Identify the blood parasite species.
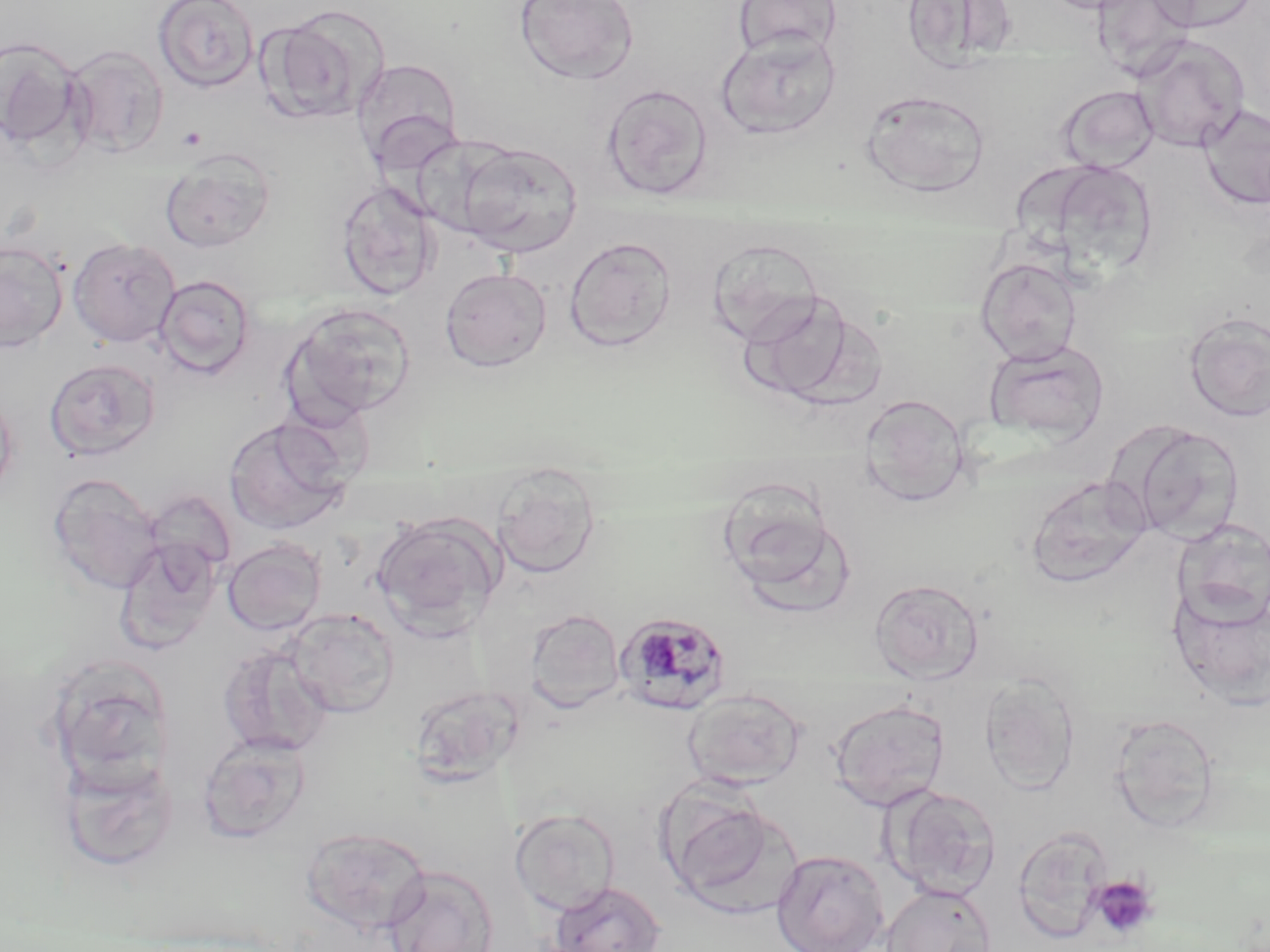

Plasmodium malariae.

Approximate bounding boxes as named x1/y1/x2/y2 corners in pixels. Plasmodium malariae-infected red blood cell locations: (x1=617, y1=611, x2=732, y2=716). Platelet locations: (x1=1087, y1=875, x2=1159, y2=942). Uninfected red blood cell locations: (x1=153, y1=0, x2=259, y2=93), (x1=514, y1=0, x2=638, y2=84), (x1=732, y1=0, x2=842, y2=59), (x1=901, y1=0, x2=1018, y2=72), (x1=1038, y1=0, x2=1149, y2=14), (x1=1091, y1=0, x2=1197, y2=81), (x1=1147, y1=0, x2=1260, y2=33), (x1=261, y1=7, x2=388, y2=126), (x1=717, y1=32, x2=841, y2=140), (x1=1132, y1=35, x2=1249, y2=152), (x1=0, y1=36, x2=85, y2=154), (x1=64, y1=44, x2=169, y2=158), (x1=350, y1=58, x2=464, y2=171), (x1=600, y1=83, x2=715, y2=200), (x1=1058, y1=85, x2=1159, y2=173), (x1=861, y1=90, x2=991, y2=197), (x1=1198, y1=104, x2=1270, y2=210), (x1=410, y1=133, x2=519, y2=238), (x1=457, y1=142, x2=583, y2=258), (x1=159, y1=148, x2=275, y2=253), (x1=1045, y1=161, x2=1158, y2=276), (x1=334, y1=180, x2=441, y2=300), (x1=563, y1=236, x2=677, y2=352), (x1=68, y1=237, x2=181, y2=348), (x1=707, y1=237, x2=824, y2=347), (x1=0, y1=239, x2=69, y2=352), (x1=975, y1=256, x2=1081, y2=366), (x1=440, y1=268, x2=552, y2=372), (x1=154, y1=275, x2=255, y2=379), (x1=743, y1=290, x2=862, y2=404), (x1=282, y1=302, x2=417, y2=423), (x1=1183, y1=312, x2=1270, y2=423), (x1=983, y1=339, x2=1110, y2=445), (x1=44, y1=358, x2=161, y2=462), (x1=0, y1=385, x2=18, y2=506), (x1=860, y1=393, x2=969, y2=506), (x1=223, y1=417, x2=351, y2=536), (x1=1119, y1=421, x2=1245, y2=544), (x1=491, y1=464, x2=601, y2=579), (x1=47, y1=472, x2=163, y2=595), (x1=1025, y1=475, x2=1154, y2=589), (x1=716, y1=484, x2=853, y2=609), (x1=371, y1=513, x2=502, y2=638), (x1=1171, y1=518, x2=1270, y2=628), (x1=115, y1=533, x2=224, y2=655), (x1=222, y1=537, x2=326, y2=636), (x1=869, y1=578, x2=984, y2=683), (x1=1167, y1=579, x2=1270, y2=710), (x1=284, y1=608, x2=400, y2=718), (x1=525, y1=609, x2=625, y2=713), (x1=218, y1=645, x2=332, y2=756), (x1=45, y1=660, x2=176, y2=789), (x1=980, y1=673, x2=1080, y2=796), (x1=409, y1=683, x2=526, y2=787), (x1=683, y1=688, x2=806, y2=789), (x1=829, y1=699, x2=950, y2=811), (x1=1108, y1=713, x2=1221, y2=832), (x1=197, y1=732, x2=311, y2=843), (x1=58, y1=753, x2=180, y2=873), (x1=885, y1=785, x2=1001, y2=900), (x1=665, y1=795, x2=797, y2=916), (x1=510, y1=808, x2=620, y2=915), (x1=1012, y1=825, x2=1112, y2=943), (x1=301, y1=826, x2=432, y2=935), (x1=771, y1=849, x2=889, y2=952), (x1=382, y1=864, x2=499, y2=952), (x1=549, y1=880, x2=667, y2=952), (x1=880, y1=884, x2=996, y2=952). Optical microscopy. Image is 1270×952 pixels. May-Grünwald-Giemsa-stained preparation. One field of a larger specimen. Thin blood smear. 1000x magnification.